Name the parasite shown.
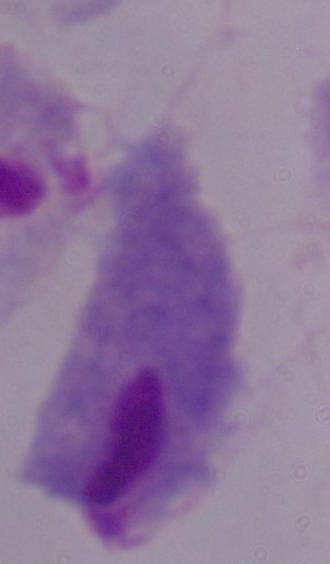
A trichomonad.

Summary:
  - Modality: micrograph
  - Magnification: 1000x